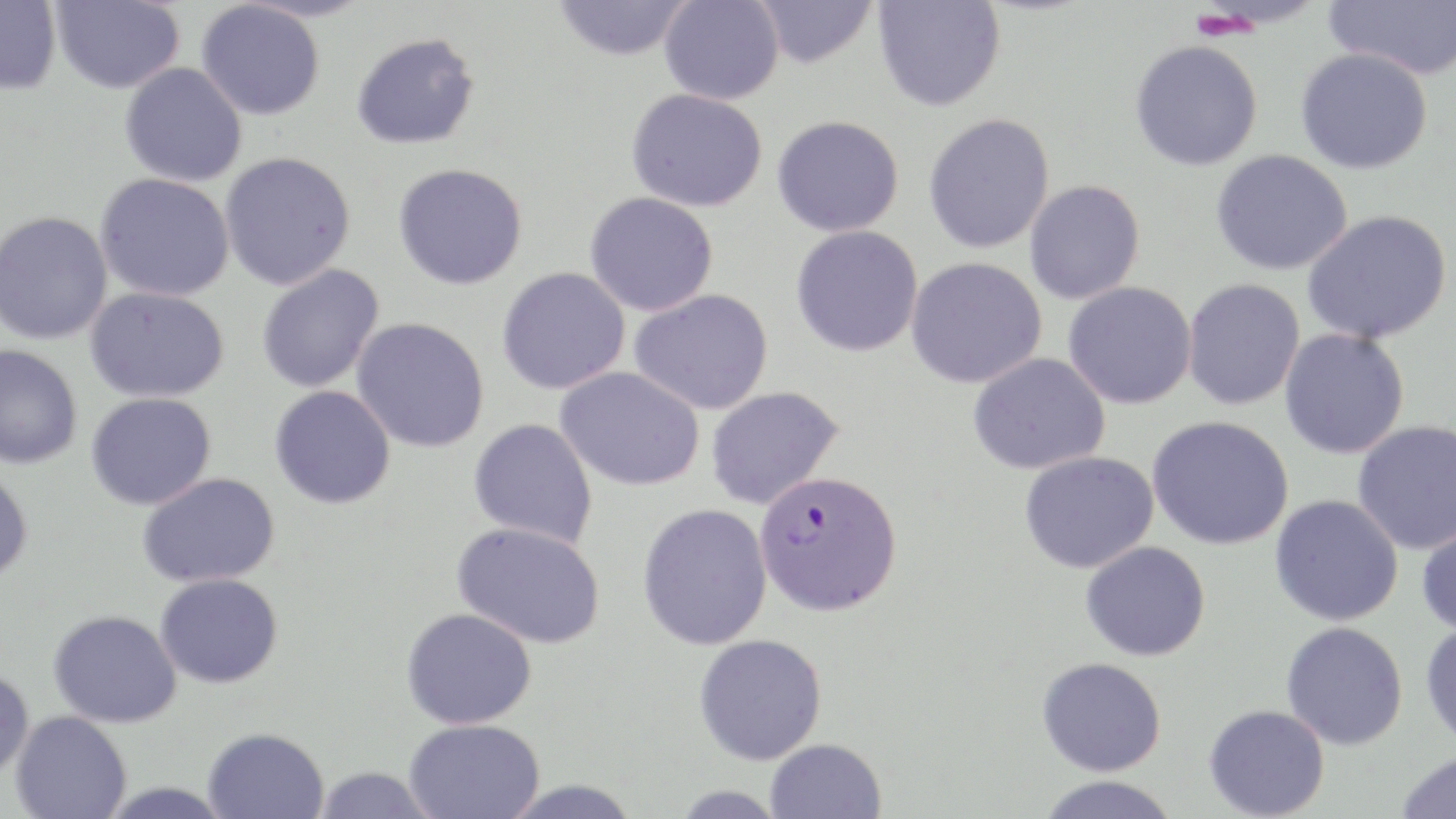

slide-level diagnosis = Plasmodium falciparum
image size = 1456×819 pixels
modality = optical microscopy
stain = May-Grünwald-Giemsa
preparation = thin blood film
field of view = one of a larger specimen
Plasmodium falciparum-infected red blood cell locations = approximate bounding boxes as [x1, y1, x2, y2] in pixels: [754, 470, 903, 617]
magnification = 1000x
uninfected red blood cell locations = approximate bounding boxes as [x1, y1, x2, y2] in pixels: [50, 0, 184, 93], [659, 0, 784, 104], [753, 0, 878, 69], [873, 0, 1005, 113], [1323, 0, 1456, 80], [0, 1, 61, 95], [196, 1, 325, 120], [553, 1, 691, 61], [351, 32, 479, 150], [1128, 40, 1264, 172], [1295, 47, 1434, 175], [119, 62, 247, 187], [625, 88, 768, 212], [923, 112, 1055, 254], [772, 115, 904, 237], [1211, 149, 1353, 275], [219, 152, 356, 290], [393, 163, 528, 290], [95, 173, 235, 302], [1024, 180, 1145, 305], [584, 192, 718, 316], [0, 210, 114, 345], [1302, 210, 1452, 343], [791, 225, 923, 357], [906, 257, 1047, 388], [256, 263, 385, 393], [497, 267, 630, 395], [1182, 278, 1305, 410], [1063, 281, 1197, 409], [85, 286, 229, 403], [629, 289, 774, 415], [351, 317, 490, 453], [1280, 328, 1410, 459], [0, 345, 83, 469], [968, 352, 1110, 475], [555, 366, 706, 492], [270, 385, 396, 509], [705, 385, 845, 510], [85, 392, 216, 510], [1147, 415, 1294, 551], [468, 418, 598, 548], [1352, 420, 1456, 555], [1019, 450, 1159, 574], [0, 468, 33, 587], [138, 472, 280, 588], [1269, 495, 1404, 626], [637, 503, 772, 650], [1416, 519, 1456, 636], [452, 521, 606, 649], [1080, 541, 1211, 661], [155, 573, 283, 689], [401, 608, 537, 731], [48, 609, 183, 728], [1280, 621, 1408, 750], [1420, 621, 1456, 749], [693, 634, 827, 766], [1037, 656, 1167, 776], [0, 667, 34, 781], [1203, 704, 1330, 818], [10, 710, 132, 819], [404, 719, 544, 819], [202, 727, 330, 818], [765, 738, 887, 819], [1395, 749, 1456, 819], [312, 766, 438, 819], [1034, 776, 1181, 819], [497, 778, 643, 818], [97, 781, 237, 819], [670, 784, 788, 818]